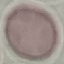

Summary:
  - Result: negative for malaria parasites
  - Stain: Giemsa
  - Capture: smartphone camera at the microscope eyepiece
  - Image type: cell patch, automatically extracted from a larger field of view and resized to 64 × 64 pixels
  - Preparation: thin smear